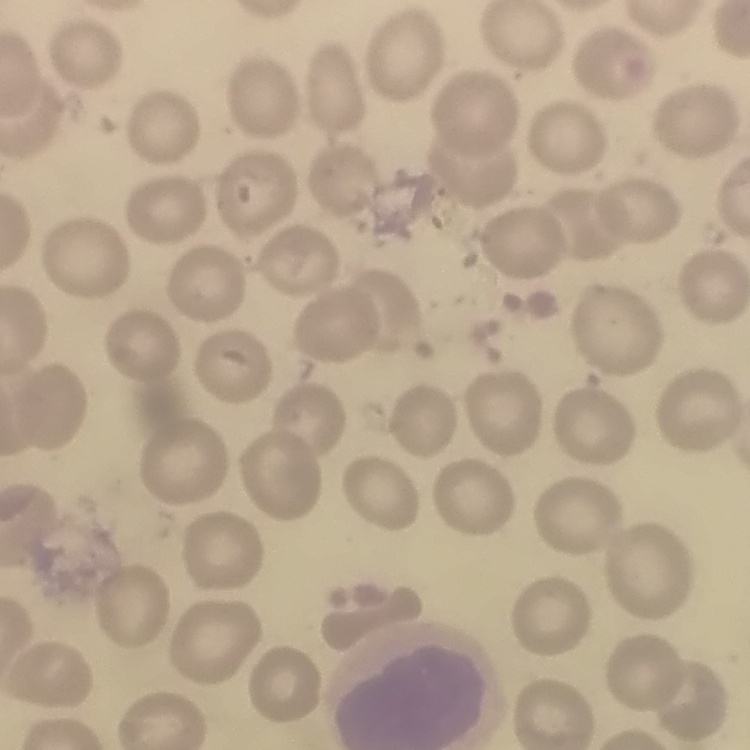

Summary:
  - Erythrocyte morphology: no rouleaux formation
  - Preparation: thin peripheral smear
  - Stain: Field's or Giemsa
  - Image type: one tile cut from a larger photomicrograph